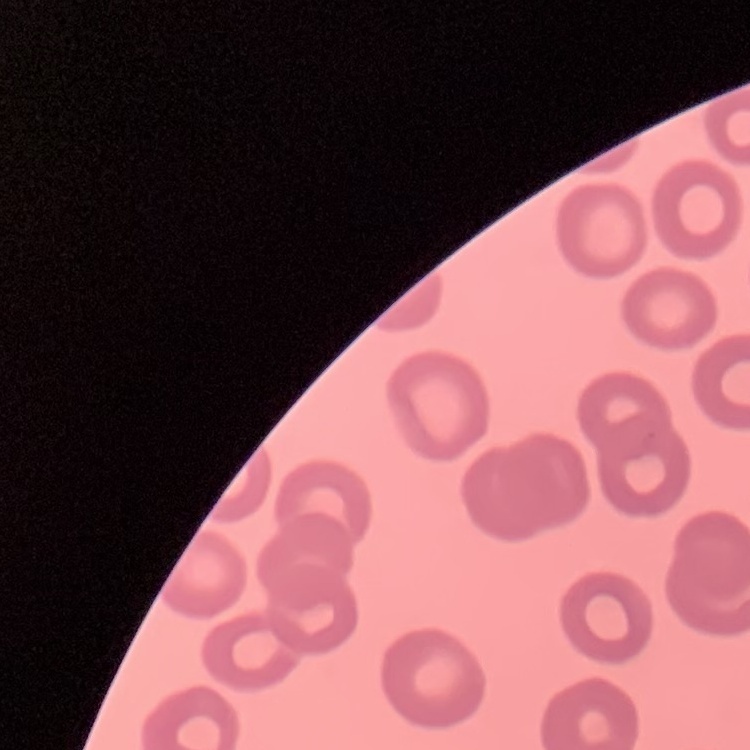
erythrocyte morphology = no rouleaux formation
image type = one tile cut from a larger photomicrograph
preparation = thin blood smear
stain = Field's or Giemsa